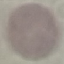

Summary:
  - Result: no malaria parasites seen
  - Preparation: thin blood film
  - Capture: smartphone camera at the microscope eyepiece
  - Image type: automatically extracted cell patch, resized to 64 × 64 pixels
  - Stain: Giemsa